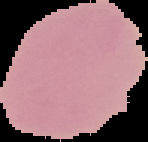
preparation = thin blood smear
result = negative for Plasmodium parasites
image size = 148×142 pixels
image type = segmented cell region on a black background